State the blood parasite species.
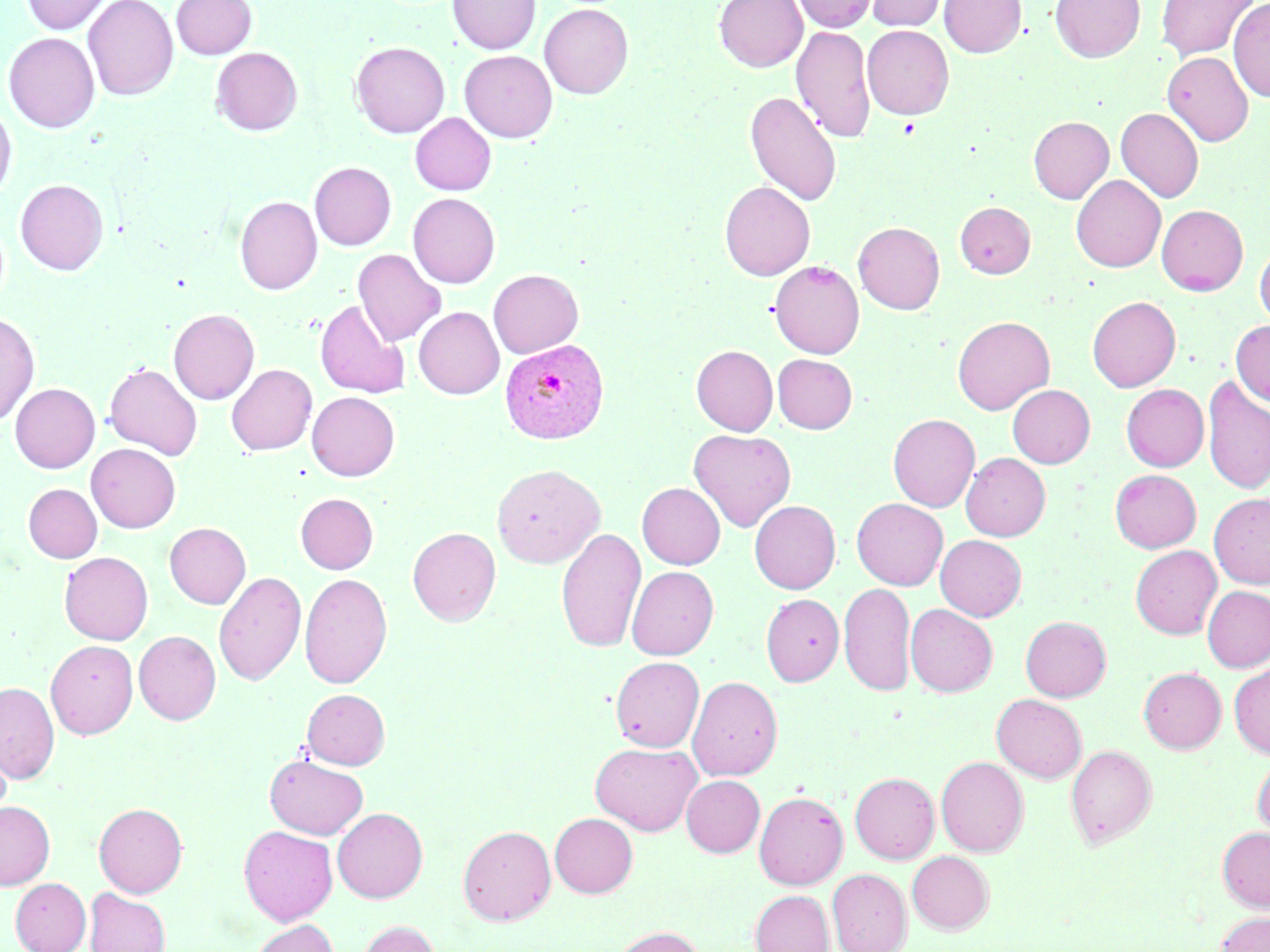
Plasmodium vivax.

Approximate bounding boxes as named x1/y1/x2/y2 corners in pixels. Plasmodium vivax-infected red blood cell locations: (x1=500, y1=338, x2=609, y2=444). Platelet locations: (x1=897, y1=117, x2=920, y2=138). Uninfected red blood cell locations: (x1=21, y1=0, x2=114, y2=35), (x1=82, y1=0, x2=179, y2=101), (x1=171, y1=0, x2=257, y2=59), (x1=448, y1=0, x2=540, y2=54), (x1=714, y1=0, x2=807, y2=72), (x1=792, y1=0, x2=877, y2=32), (x1=866, y1=0, x2=948, y2=32), (x1=939, y1=0, x2=1025, y2=58), (x1=1050, y1=0, x2=1145, y2=62), (x1=1155, y1=0, x2=1259, y2=62), (x1=1228, y1=0, x2=1270, y2=102), (x1=539, y1=4, x2=633, y2=99), (x1=791, y1=25, x2=875, y2=143), (x1=862, y1=25, x2=954, y2=119), (x1=3, y1=31, x2=100, y2=132), (x1=351, y1=41, x2=449, y2=138), (x1=211, y1=47, x2=302, y2=135), (x1=459, y1=50, x2=557, y2=142), (x1=1162, y1=52, x2=1254, y2=146), (x1=745, y1=91, x2=842, y2=207), (x1=0, y1=101, x2=17, y2=202), (x1=1116, y1=108, x2=1204, y2=203), (x1=410, y1=112, x2=496, y2=195), (x1=1028, y1=116, x2=1114, y2=203), (x1=309, y1=161, x2=396, y2=250), (x1=1071, y1=174, x2=1166, y2=272), (x1=15, y1=179, x2=108, y2=275), (x1=719, y1=181, x2=815, y2=280), (x1=408, y1=193, x2=500, y2=288), (x1=235, y1=195, x2=322, y2=295), (x1=955, y1=201, x2=1035, y2=279), (x1=1156, y1=205, x2=1248, y2=295), (x1=853, y1=222, x2=945, y2=314), (x1=1254, y1=241, x2=1270, y2=329), (x1=353, y1=249, x2=446, y2=346), (x1=769, y1=260, x2=864, y2=359), (x1=488, y1=269, x2=583, y2=358), (x1=1087, y1=296, x2=1181, y2=392), (x1=314, y1=300, x2=410, y2=398), (x1=413, y1=307, x2=504, y2=399), (x1=168, y1=309, x2=259, y2=405), (x1=0, y1=312, x2=39, y2=426), (x1=953, y1=316, x2=1055, y2=414), (x1=1231, y1=320, x2=1270, y2=406), (x1=691, y1=345, x2=778, y2=435), (x1=772, y1=354, x2=858, y2=433), (x1=104, y1=362, x2=202, y2=460), (x1=226, y1=364, x2=317, y2=455), (x1=1201, y1=375, x2=1270, y2=495), (x1=10, y1=383, x2=100, y2=473), (x1=1121, y1=384, x2=1209, y2=471), (x1=1007, y1=385, x2=1095, y2=468), (x1=307, y1=391, x2=400, y2=481), (x1=888, y1=414, x2=980, y2=512), (x1=689, y1=429, x2=796, y2=532), (x1=86, y1=443, x2=180, y2=533), (x1=960, y1=453, x2=1050, y2=540), (x1=491, y1=463, x2=605, y2=568), (x1=1110, y1=469, x2=1201, y2=552), (x1=23, y1=483, x2=102, y2=563), (x1=637, y1=483, x2=725, y2=569), (x1=1209, y1=492, x2=1270, y2=588), (x1=295, y1=493, x2=378, y2=574), (x1=851, y1=498, x2=948, y2=590), (x1=750, y1=500, x2=840, y2=593), (x1=165, y1=522, x2=251, y2=608), (x1=407, y1=527, x2=501, y2=625), (x1=556, y1=527, x2=646, y2=654), (x1=935, y1=535, x2=1026, y2=621), (x1=1130, y1=545, x2=1222, y2=638), (x1=59, y1=551, x2=153, y2=645), (x1=626, y1=566, x2=718, y2=659), (x1=213, y1=571, x2=306, y2=687), (x1=300, y1=573, x2=392, y2=688), (x1=839, y1=582, x2=915, y2=697), (x1=1202, y1=586, x2=1270, y2=672), (x1=760, y1=593, x2=844, y2=686), (x1=905, y1=603, x2=998, y2=696), (x1=1020, y1=616, x2=1111, y2=701), (x1=134, y1=630, x2=221, y2=725), (x1=45, y1=640, x2=138, y2=739), (x1=610, y1=656, x2=704, y2=752), (x1=1229, y1=664, x2=1270, y2=759), (x1=1138, y1=667, x2=1226, y2=753), (x1=687, y1=676, x2=783, y2=780), (x1=0, y1=681, x2=59, y2=783), (x1=302, y1=688, x2=390, y2=769), (x1=991, y1=694, x2=1087, y2=783), (x1=590, y1=742, x2=702, y2=835), (x1=1066, y1=744, x2=1157, y2=849), (x1=264, y1=754, x2=368, y2=839), (x1=1252, y1=754, x2=1270, y2=836), (x1=936, y1=756, x2=1028, y2=856), (x1=850, y1=772, x2=939, y2=863), (x1=681, y1=775, x2=765, y2=857), (x1=754, y1=791, x2=848, y2=890), (x1=0, y1=801, x2=55, y2=890), (x1=93, y1=802, x2=187, y2=897), (x1=332, y1=807, x2=428, y2=902), (x1=550, y1=813, x2=638, y2=897), (x1=239, y1=825, x2=338, y2=925), (x1=458, y1=825, x2=556, y2=925), (x1=1217, y1=827, x2=1270, y2=911), (x1=906, y1=851, x2=994, y2=934), (x1=827, y1=869, x2=911, y2=952), (x1=11, y1=877, x2=90, y2=952), (x1=85, y1=888, x2=169, y2=952), (x1=750, y1=890, x2=833, y2=952), (x1=1215, y1=912, x2=1270, y2=952), (x1=248, y1=919, x2=339, y2=952), (x1=360, y1=920, x2=440, y2=952), (x1=612, y1=926, x2=704, y2=952). Single field of view. May-Grünwald-Giemsa stain. Thin blood smear. Image is 1270×952 pixels. 1000x magnification. Optical microscopy.